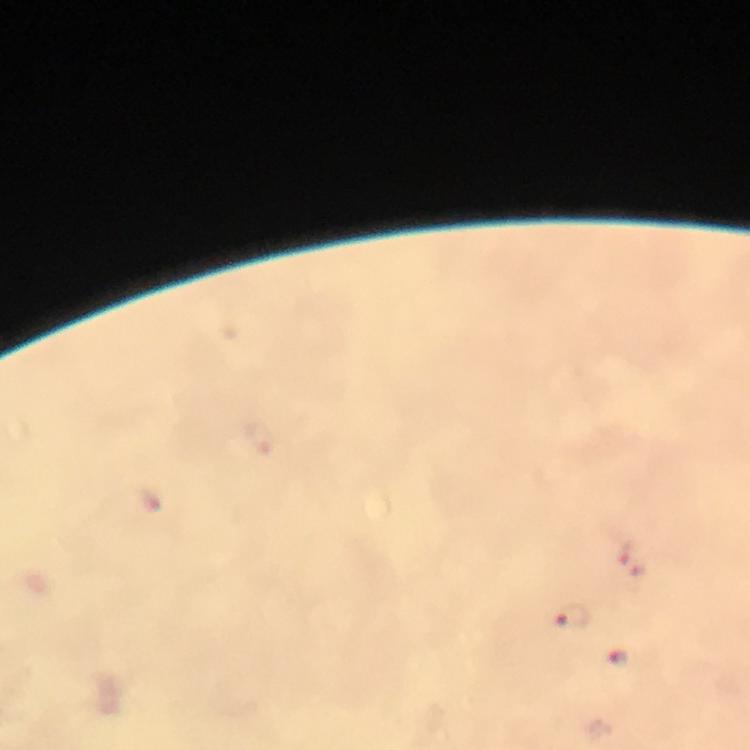

preparation: thick blood film
malaria_parasite_locations: 'approximate centers as (x, y) in pixels: (630, 561), (569, 616), (617, 657)'
capture: smartphone photograph through a microscope
magnification: 100x
cropped_from: a single field of view
stain: Giemsa
image_size: 750×750 pixels
context: from a malaria diagnostic workup
immersion_oil: used